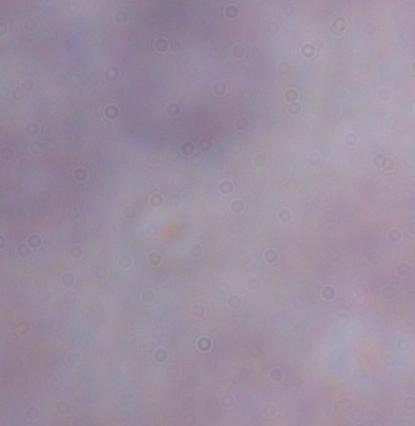

{
  "identification": "trypanosome",
  "modality": "photomicrograph",
  "magnification": "1000x"
}